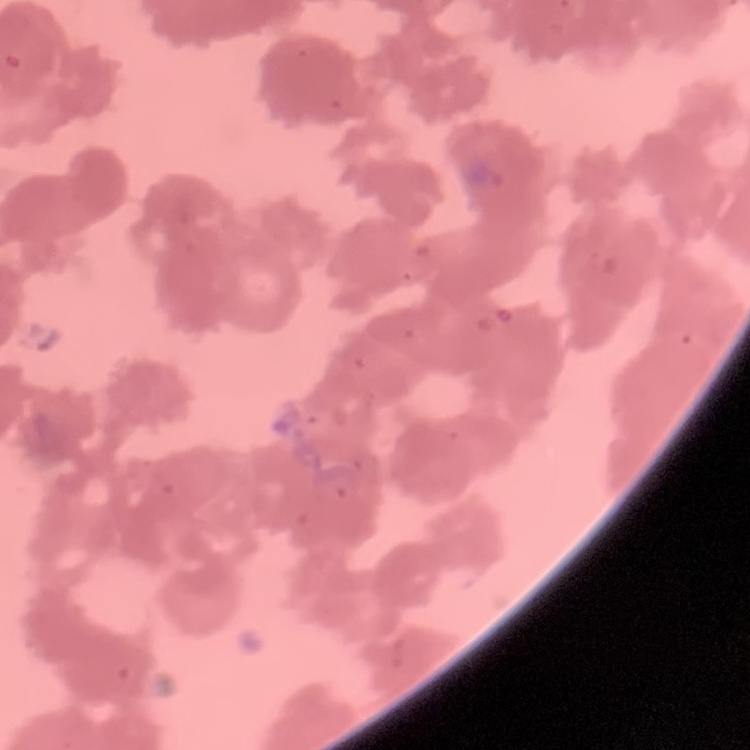
The red blood cells show rouleaux formation. One tile cut from a larger photomicrograph. Thin blood smear. Stained with either Field's or Giemsa.